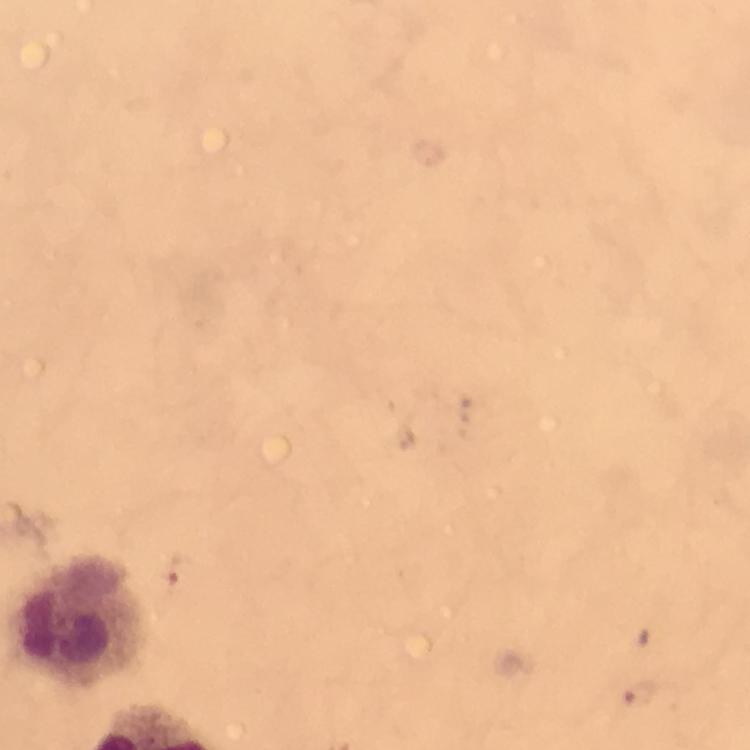
malaria parasite locations = approximate centers as {x, y} in pixels: {640, 693}
context = from a diagnostic examination for malaria
cropped from = a single field of view
preparation = thick blood film
image size = 750×750 pixels
capture = smartphone camera through the microscope
leukocyte locations = approximate centers as {x, y} in pixels: {81, 620}
stain = Giemsa
magnification = 100x
immersion oil = applied